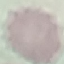
Result: no malaria parasites detected. Acquired by smartphone through the microscope eyepiece. Automatically extracted cell patch, resized to 64 × 64 pixels. Thin blood smear. Giemsa-stained preparation.